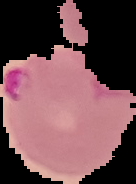
Summary:
  - Image type: segmented cell region with the area outside set to black
  - Malaria status: parasitized
  - Preparation: thin blood film
  - Image size: 136×184 pixels